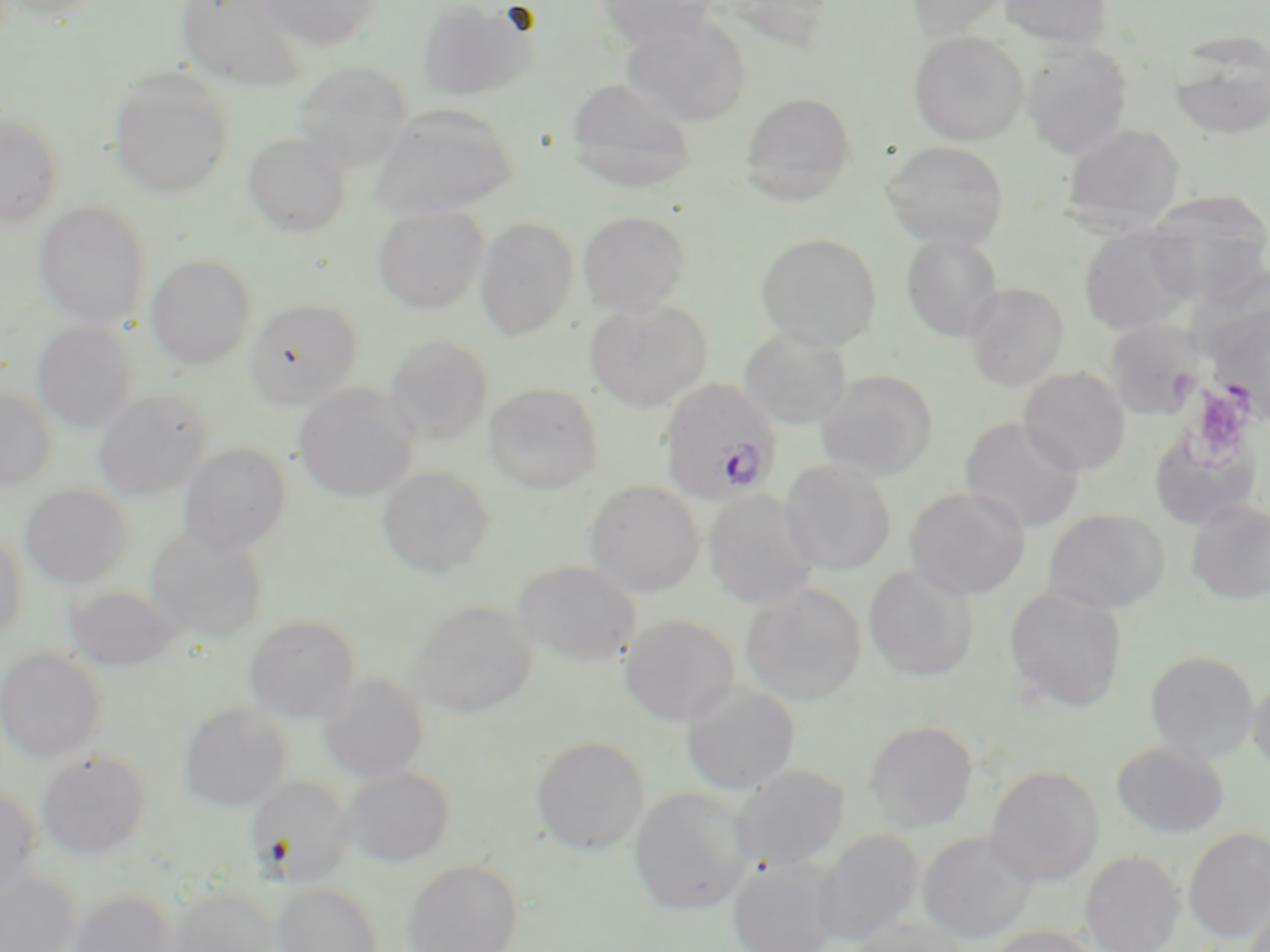
Summary:
  - Coordinate format: approximate bounding boxes as named x1/y1/x2/y2 corners in pixels
  - Platelet locations: (x1=1188, y1=383, x2=1255, y2=460)
  - Uninfected red blood cell locations: (x1=4, y1=0, x2=104, y2=22), (x1=176, y1=0, x2=307, y2=91), (x1=257, y1=0, x2=383, y2=51), (x1=417, y1=0, x2=535, y2=101), (x1=594, y1=0, x2=717, y2=49), (x1=716, y1=0, x2=835, y2=52), (x1=905, y1=0, x2=1017, y2=39), (x1=999, y1=0, x2=1112, y2=49), (x1=619, y1=15, x2=751, y2=127), (x1=909, y1=31, x2=1028, y2=145), (x1=1168, y1=31, x2=1270, y2=139), (x1=1021, y1=40, x2=1134, y2=159), (x1=292, y1=61, x2=413, y2=170), (x1=108, y1=70, x2=233, y2=198), (x1=566, y1=79, x2=697, y2=193), (x1=740, y1=91, x2=856, y2=203), (x1=371, y1=103, x2=518, y2=218), (x1=0, y1=114, x2=64, y2=226), (x1=1060, y1=124, x2=1186, y2=231), (x1=243, y1=132, x2=351, y2=237), (x1=882, y1=141, x2=1009, y2=251), (x1=1144, y1=190, x2=1270, y2=295), (x1=33, y1=202, x2=150, y2=330), (x1=372, y1=205, x2=489, y2=314), (x1=578, y1=211, x2=691, y2=316), (x1=474, y1=217, x2=578, y2=341), (x1=1079, y1=227, x2=1195, y2=336), (x1=756, y1=232, x2=882, y2=350), (x1=901, y1=232, x2=1005, y2=341), (x1=146, y1=255, x2=256, y2=370), (x1=965, y1=283, x2=1069, y2=391), (x1=246, y1=299, x2=361, y2=408), (x1=584, y1=300, x2=712, y2=411), (x1=1206, y1=307, x2=1270, y2=423), (x1=1104, y1=320, x2=1205, y2=418), (x1=30, y1=321, x2=138, y2=432), (x1=740, y1=329, x2=852, y2=428), (x1=385, y1=335, x2=494, y2=445), (x1=1019, y1=367, x2=1131, y2=475), (x1=816, y1=370, x2=938, y2=480), (x1=484, y1=383, x2=603, y2=494), (x1=293, y1=384, x2=418, y2=502), (x1=0, y1=388, x2=57, y2=489), (x1=92, y1=389, x2=213, y2=501), (x1=960, y1=416, x2=1085, y2=533), (x1=1148, y1=428, x2=1262, y2=531), (x1=179, y1=442, x2=292, y2=555), (x1=780, y1=460, x2=897, y2=575), (x1=378, y1=465, x2=495, y2=578), (x1=585, y1=480, x2=704, y2=597), (x1=20, y1=485, x2=133, y2=589), (x1=905, y1=486, x2=1030, y2=600), (x1=702, y1=489, x2=820, y2=610), (x1=1186, y1=500, x2=1270, y2=604), (x1=1043, y1=509, x2=1170, y2=614), (x1=145, y1=525, x2=268, y2=644), (x1=0, y1=531, x2=27, y2=645), (x1=513, y1=561, x2=642, y2=665), (x1=863, y1=565, x2=978, y2=680), (x1=740, y1=584, x2=867, y2=707), (x1=63, y1=586, x2=182, y2=673), (x1=1005, y1=586, x2=1127, y2=713), (x1=407, y1=601, x2=538, y2=718), (x1=619, y1=614, x2=739, y2=726), (x1=244, y1=615, x2=360, y2=723), (x1=0, y1=648, x2=107, y2=763), (x1=1145, y1=650, x2=1260, y2=764), (x1=318, y1=672, x2=429, y2=783), (x1=1248, y1=674, x2=1270, y2=776), (x1=681, y1=684, x2=800, y2=795), (x1=177, y1=702, x2=291, y2=811), (x1=864, y1=720, x2=977, y2=832), (x1=531, y1=736, x2=650, y2=855), (x1=1111, y1=741, x2=1228, y2=838), (x1=36, y1=751, x2=152, y2=860), (x1=730, y1=765, x2=850, y2=872), (x1=985, y1=765, x2=1104, y2=887), (x1=340, y1=766, x2=455, y2=867), (x1=245, y1=776, x2=354, y2=888), (x1=629, y1=786, x2=755, y2=916), (x1=0, y1=787, x2=42, y2=899), (x1=1183, y1=827, x2=1270, y2=944), (x1=811, y1=829, x2=925, y2=948), (x1=918, y1=832, x2=1037, y2=945), (x1=1079, y1=850, x2=1186, y2=952), (x1=727, y1=857, x2=841, y2=952), (x1=402, y1=859, x2=523, y2=952), (x1=0, y1=865, x2=80, y2=952), (x1=272, y1=883, x2=383, y2=952), (x1=164, y1=886, x2=279, y2=952), (x1=1242, y1=889, x2=1269, y2=952), (x1=67, y1=890, x2=176, y2=952), (x1=844, y1=919, x2=972, y2=952), (x1=985, y1=925, x2=1102, y2=952)
  - Plasmodium ovale-infected red blood cell locations: (x1=658, y1=378, x2=783, y2=505)
  - Slide-level diagnosis: Plasmodium ovale
  - Image size: 1270×952 pixels
  - Magnification: 1000x
  - Field of view: single
  - Stain: May-Grünwald-Giemsa
  - Modality: optical microscopy
  - Preparation: thin blood smear